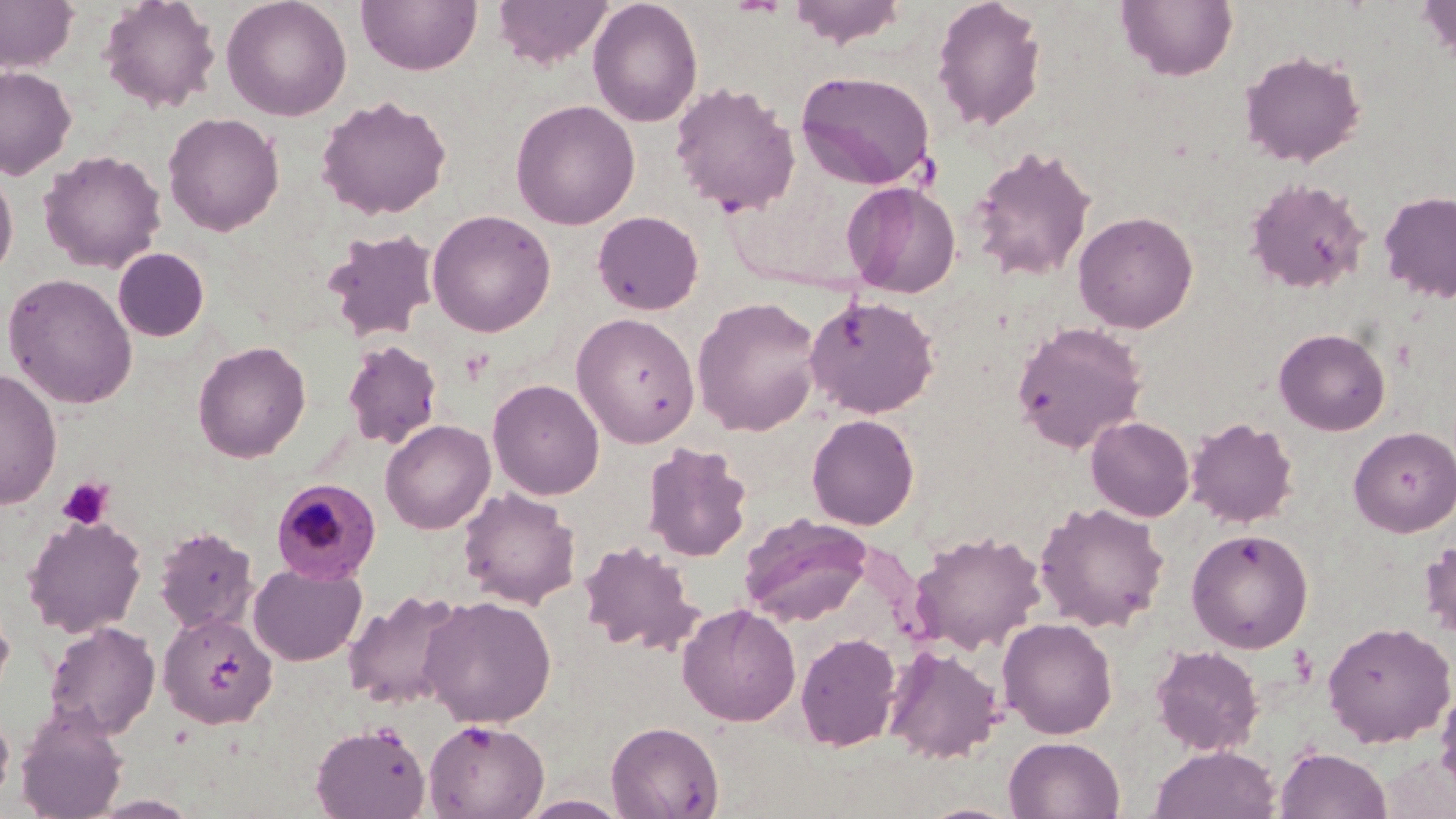 Approximate bounding boxes as (x1,y1)-(x2,y2) corner pairs in pixels. Platelet locations: (56,477)-(114,530). Plasmodium malariae-infected red blood cell locations: (270,478)-(381,584). Uninfected red blood cell locations: (0,0)-(80,73), (98,0)-(221,113), (221,0)-(352,121), (357,0)-(481,75), (492,0)-(614,69), (587,0)-(703,127), (786,0)-(911,49), (931,0)-(1047,133), (1116,0)-(1238,82), (1415,0)-(1456,68), (1239,49)-(1366,168), (0,66)-(76,179), (796,70)-(937,191), (669,81)-(800,216), (316,94)-(452,220), (510,99)-(640,230), (163,112)-(284,236), (969,144)-(1096,282), (39,149)-(167,273), (0,164)-(18,283), (1244,176)-(1371,295), (841,181)-(961,298), (1378,190)-(1456,302), (427,209)-(556,337), (593,210)-(704,315), (1073,210)-(1198,334), (322,229)-(439,342), (112,248)-(210,342), (2,272)-(138,409), (804,294)-(939,418), (691,296)-(823,436), (571,313)-(700,447), (1011,320)-(1148,453), (1274,328)-(1391,435), (342,339)-(443,449), (192,340)-(311,462), (0,369)-(62,509), (487,378)-(605,500), (806,414)-(919,530), (1086,416)-(1194,521), (1185,416)-(1299,528), (380,419)-(496,534), (1349,426)-(1456,537), (642,440)-(752,562), (457,487)-(581,609), (1035,501)-(1170,632), (736,511)-(881,629), (22,515)-(148,638), (153,526)-(259,635), (1186,528)-(1313,653), (911,529)-(1046,655), (1419,538)-(1456,641), (578,539)-(702,654), (248,562)-(366,666), (342,589)-(469,711), (419,595)-(557,727), (0,597)-(15,707), (677,603)-(801,726), (157,611)-(278,729), (997,617)-(1118,739), (1322,620)-(1455,747), (44,621)-(161,738), (795,631)-(902,751), (1151,644)-(1264,756), (884,645)-(1004,763), (1435,681)-(1456,800), (15,703)-(128,819), (0,706)-(15,808), (422,719)-(549,818), (606,720)-(723,818), (310,722)-(431,818), (1003,736)-(1125,818), (1149,745)-(1281,819), (1275,746)-(1391,819), (517,794)-(631,818). Slide-level diagnosis: Plasmodium malariae. Captured at 1000x magnification. Optical microscopy. May-Grünwald-Giemsa stain. Image is 1456×819 pixels. Thin blood film. Single field of view.